Comment on the morphology of the erythrocytes.
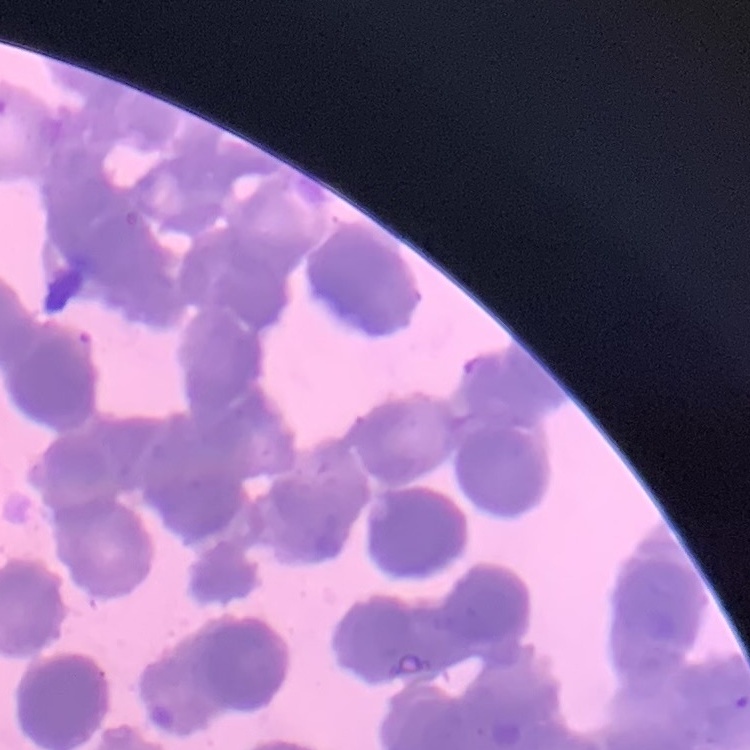

They show rouleaux formation.

Field's or Giemsa stain. Thin blood smear. One tile cut from a larger photomicrograph.